State the blood parasite species.
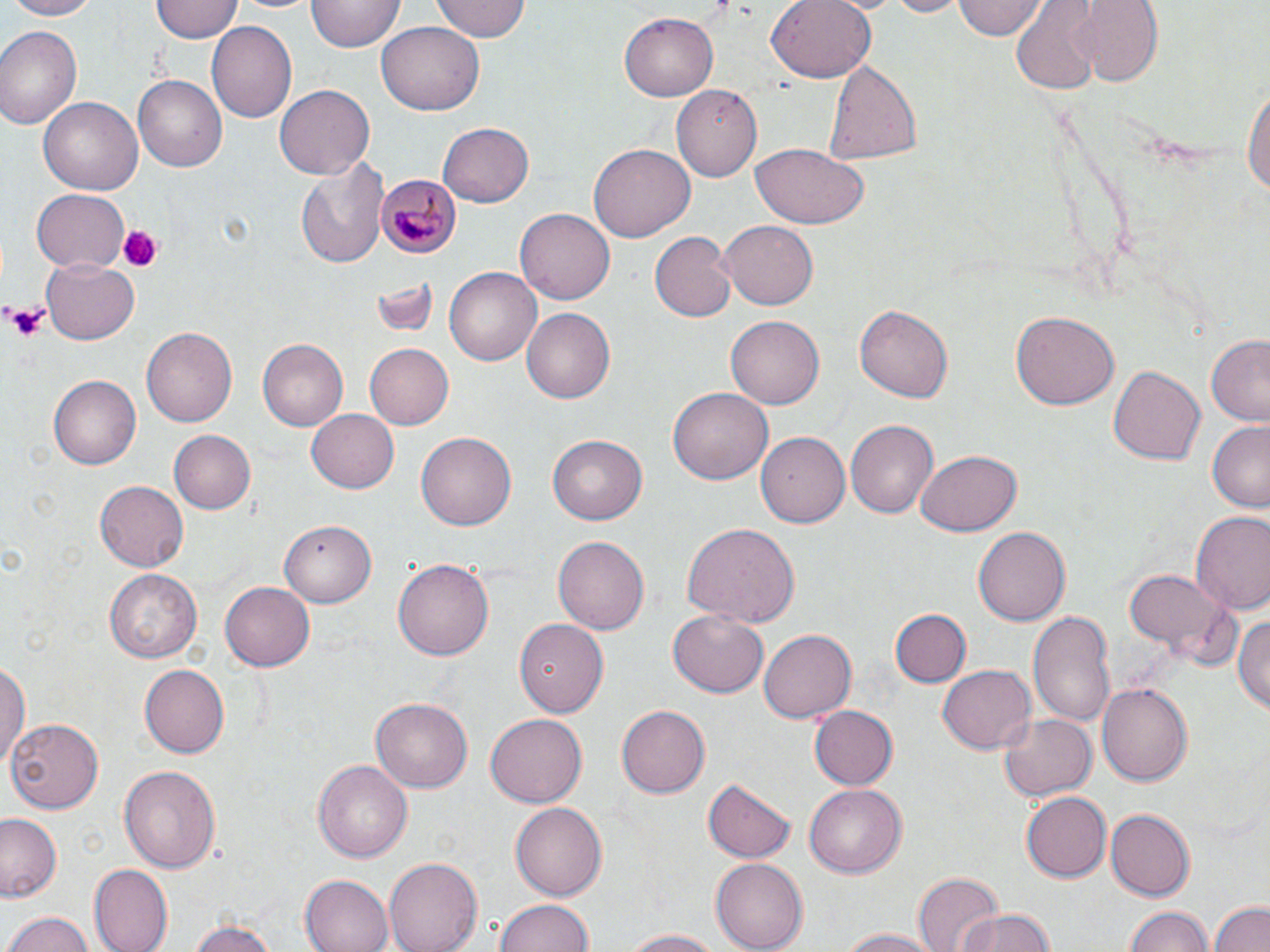

Plasmodium malariae.

Approximate bounding boxes as named x1/y1/x2/y2 corners in pixels. Uninfected red blood cell locations: (x1=5, y1=0, x2=102, y2=21), (x1=152, y1=0, x2=242, y2=42), (x1=228, y1=0, x2=321, y2=15), (x1=433, y1=0, x2=530, y2=42), (x1=765, y1=0, x2=876, y2=82), (x1=875, y1=0, x2=974, y2=18), (x1=956, y1=0, x2=1045, y2=41), (x1=1068, y1=0, x2=1167, y2=86), (x1=307, y1=1, x2=404, y2=54), (x1=1013, y1=5, x2=1103, y2=88), (x1=619, y1=10, x2=722, y2=101), (x1=207, y1=21, x2=299, y2=121), (x1=377, y1=24, x2=485, y2=115), (x1=0, y1=25, x2=83, y2=130), (x1=822, y1=61, x2=925, y2=162), (x1=135, y1=76, x2=226, y2=171), (x1=1243, y1=77, x2=1269, y2=207), (x1=675, y1=84, x2=763, y2=182), (x1=276, y1=85, x2=375, y2=178), (x1=39, y1=97, x2=142, y2=196), (x1=438, y1=122, x2=534, y2=205), (x1=589, y1=143, x2=695, y2=241), (x1=750, y1=145, x2=870, y2=229), (x1=295, y1=158, x2=387, y2=268), (x1=30, y1=188, x2=130, y2=273), (x1=517, y1=208, x2=615, y2=302), (x1=717, y1=220, x2=819, y2=311), (x1=648, y1=231, x2=735, y2=323), (x1=40, y1=259, x2=139, y2=343), (x1=444, y1=267, x2=541, y2=365), (x1=370, y1=277, x2=436, y2=338), (x1=855, y1=301, x2=954, y2=402), (x1=521, y1=308, x2=616, y2=404), (x1=1011, y1=311, x2=1118, y2=409), (x1=725, y1=317, x2=822, y2=410), (x1=141, y1=327, x2=239, y2=428), (x1=1202, y1=331, x2=1270, y2=427), (x1=258, y1=340, x2=347, y2=429), (x1=365, y1=344, x2=454, y2=428), (x1=1107, y1=364, x2=1206, y2=467), (x1=49, y1=374, x2=145, y2=469), (x1=670, y1=387, x2=772, y2=485), (x1=307, y1=408, x2=401, y2=493), (x1=846, y1=420, x2=938, y2=519), (x1=1207, y1=421, x2=1270, y2=513), (x1=168, y1=429, x2=256, y2=514), (x1=757, y1=431, x2=850, y2=527), (x1=417, y1=433, x2=516, y2=530), (x1=548, y1=435, x2=647, y2=525), (x1=916, y1=451, x2=1021, y2=536), (x1=94, y1=481, x2=189, y2=571), (x1=1192, y1=514, x2=1270, y2=617), (x1=280, y1=518, x2=375, y2=606), (x1=682, y1=522, x2=799, y2=630), (x1=973, y1=527, x2=1071, y2=626), (x1=553, y1=537, x2=650, y2=633), (x1=392, y1=557, x2=493, y2=661), (x1=105, y1=569, x2=201, y2=663), (x1=1122, y1=569, x2=1229, y2=658), (x1=220, y1=580, x2=314, y2=672), (x1=888, y1=608, x2=971, y2=689), (x1=1027, y1=608, x2=1117, y2=730), (x1=1234, y1=610, x2=1270, y2=718), (x1=669, y1=611, x2=767, y2=697), (x1=515, y1=618, x2=609, y2=717), (x1=758, y1=628, x2=855, y2=724), (x1=0, y1=662, x2=28, y2=769), (x1=138, y1=664, x2=229, y2=759), (x1=938, y1=664, x2=1036, y2=754), (x1=1097, y1=681, x2=1195, y2=785), (x1=370, y1=695, x2=472, y2=789), (x1=615, y1=705, x2=710, y2=799), (x1=809, y1=705, x2=898, y2=789), (x1=995, y1=710, x2=1099, y2=804), (x1=484, y1=714, x2=586, y2=808), (x1=8, y1=717, x2=104, y2=811), (x1=312, y1=758, x2=413, y2=862), (x1=119, y1=764, x2=220, y2=876), (x1=703, y1=778, x2=798, y2=862), (x1=804, y1=783, x2=907, y2=878), (x1=1022, y1=791, x2=1112, y2=881), (x1=509, y1=800, x2=608, y2=900), (x1=1105, y1=808, x2=1194, y2=902), (x1=0, y1=814, x2=61, y2=900), (x1=382, y1=856, x2=484, y2=952), (x1=710, y1=860, x2=808, y2=951), (x1=89, y1=865, x2=172, y2=951), (x1=912, y1=873, x2=1004, y2=952), (x1=300, y1=874, x2=394, y2=952), (x1=495, y1=899, x2=597, y2=952), (x1=1209, y1=900, x2=1270, y2=952), (x1=1123, y1=906, x2=1216, y2=952), (x1=6, y1=909, x2=96, y2=952), (x1=952, y1=910, x2=1060, y2=952), (x1=185, y1=918, x2=286, y2=951), (x1=840, y1=927, x2=949, y2=951), (x1=620, y1=928, x2=731, y2=950). Platelet locations: (x1=116, y1=224, x2=163, y2=273), (x1=4, y1=303, x2=52, y2=342). Plasmodium malariae-infected red blood cell locations: (x1=377, y1=171, x2=461, y2=260). Thin blood smear. 1000x magnification. One field of a larger specimen. Optical microscopy. May-Grünwald-Giemsa stain. Image is 1270×952 pixels.